Give the position of every malaria parasite.
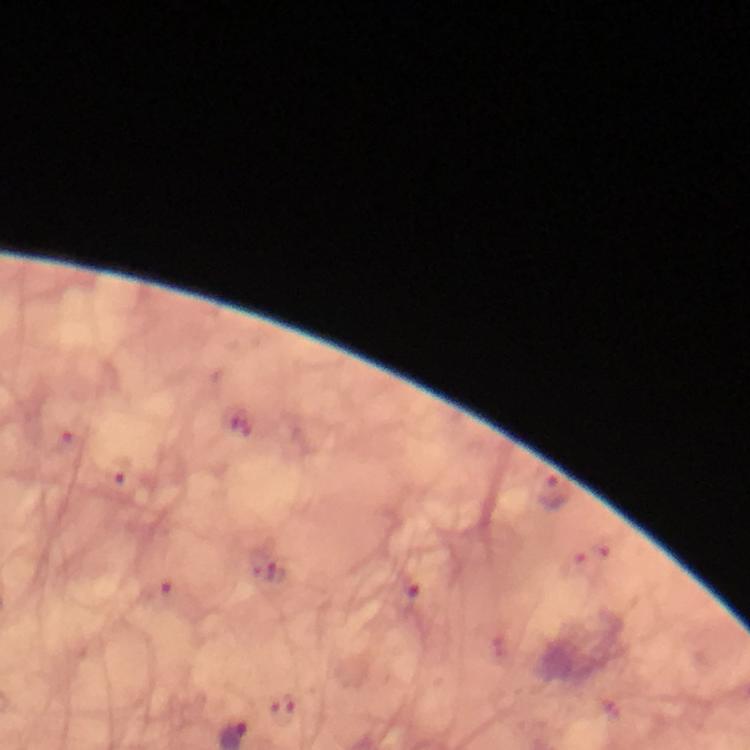

Approximate object centers, in pixels from the top-left corner.
Malaria parasites: (x=408, y=596).

image_size: 750×750 pixels
immersion_oil: used
context: from a malaria diagnostic workup
preparation: thick blood smear
magnification: 100x
capture: smartphone photograph through a microscope
cropped_from: one field of view
stain: Giemsa